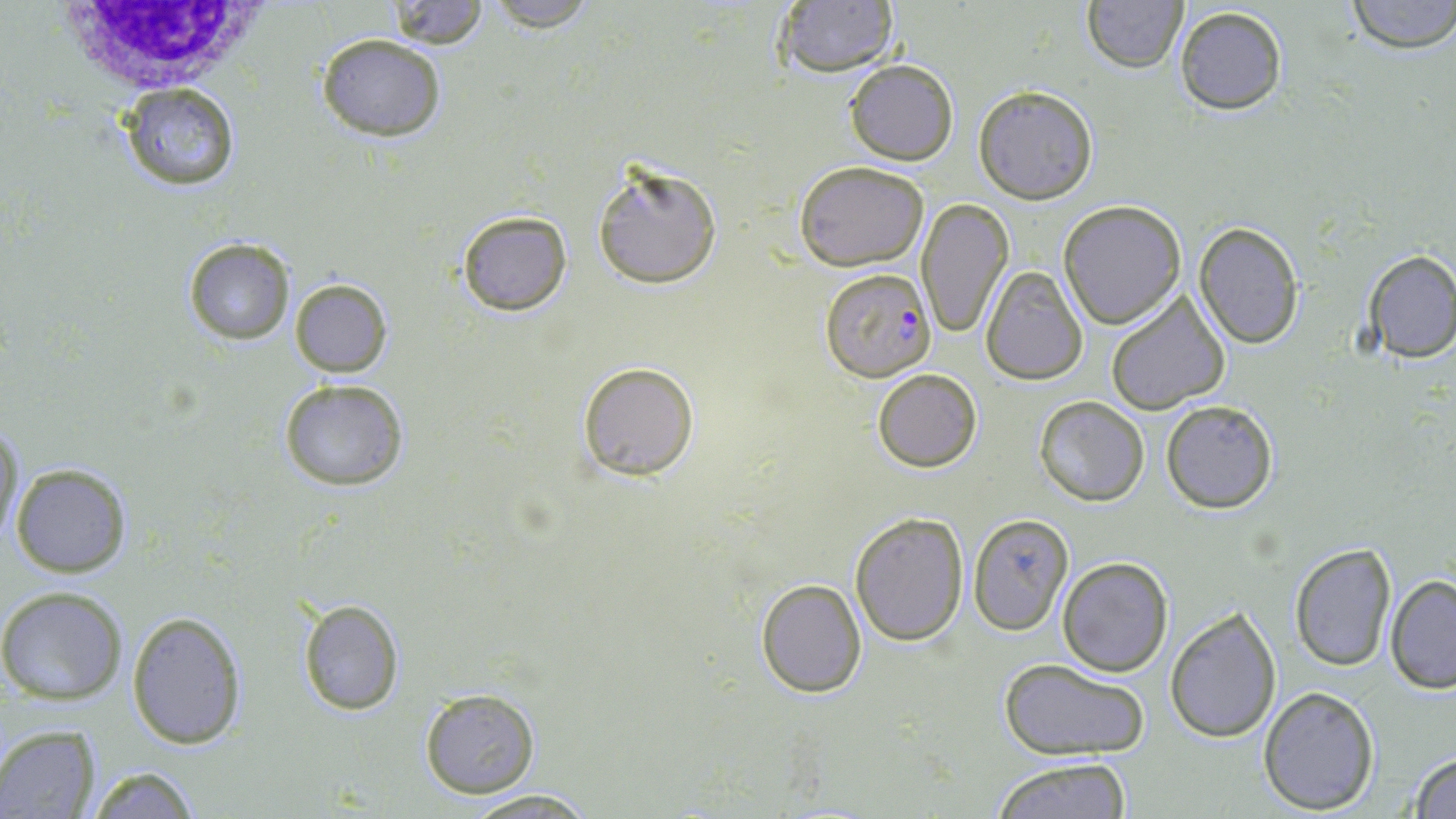

Approximate bounding boxes as (x1,y1)-(x2,y2) corner pairs in pixels. Plasmodium falciparum-infected red blood cell locations: (820,267)-(936,381). Uninfected red blood cell locations: (387,0)-(488,47), (480,0)-(601,30), (1081,0)-(1188,74), (1343,0)-(1456,52), (770,1)-(900,79), (1173,6)-(1288,115), (317,33)-(445,140), (845,59)-(958,166), (116,83)-(240,192), (974,85)-(1098,204), (591,161)-(721,292), (794,161)-(929,270), (917,199)-(1012,338), (1058,200)-(1186,329), (456,210)-(573,316), (1192,222)-(1303,350), (184,238)-(295,345), (1359,248)-(1455,363), (980,266)-(1088,384), (290,278)-(391,377), (1105,291)-(1230,415), (576,360)-(701,481), (872,367)-(982,473), (281,380)-(407,491), (1033,395)-(1149,506), (1160,398)-(1281,515), (1,418)-(24,543), (10,461)-(135,577), (849,510)-(967,648), (962,511)-(1075,636), (1287,541)-(1397,672), (1056,557)-(1174,676), (1385,575)-(1456,694), (756,579)-(866,697), (0,587)-(127,703), (296,597)-(406,716), (1165,607)-(1283,745), (127,609)-(248,751), (1001,657)-(1151,762), (1258,686)-(1380,814), (419,688)-(541,799), (0,726)-(100,818), (1408,752)-(1456,819), (992,757)-(1137,818), (86,765)-(201,819), (462,789)-(599,819). White blood cell locations: (58,0)-(258,96). Slide-level diagnosis: Plasmodium falciparum. Light microscopy. Image is 1456×819 pixels. One field of a larger specimen. Captured at 1000x magnification. Thin blood smear. May-Grünwald-Giemsa-stained preparation.